State the preparation type.
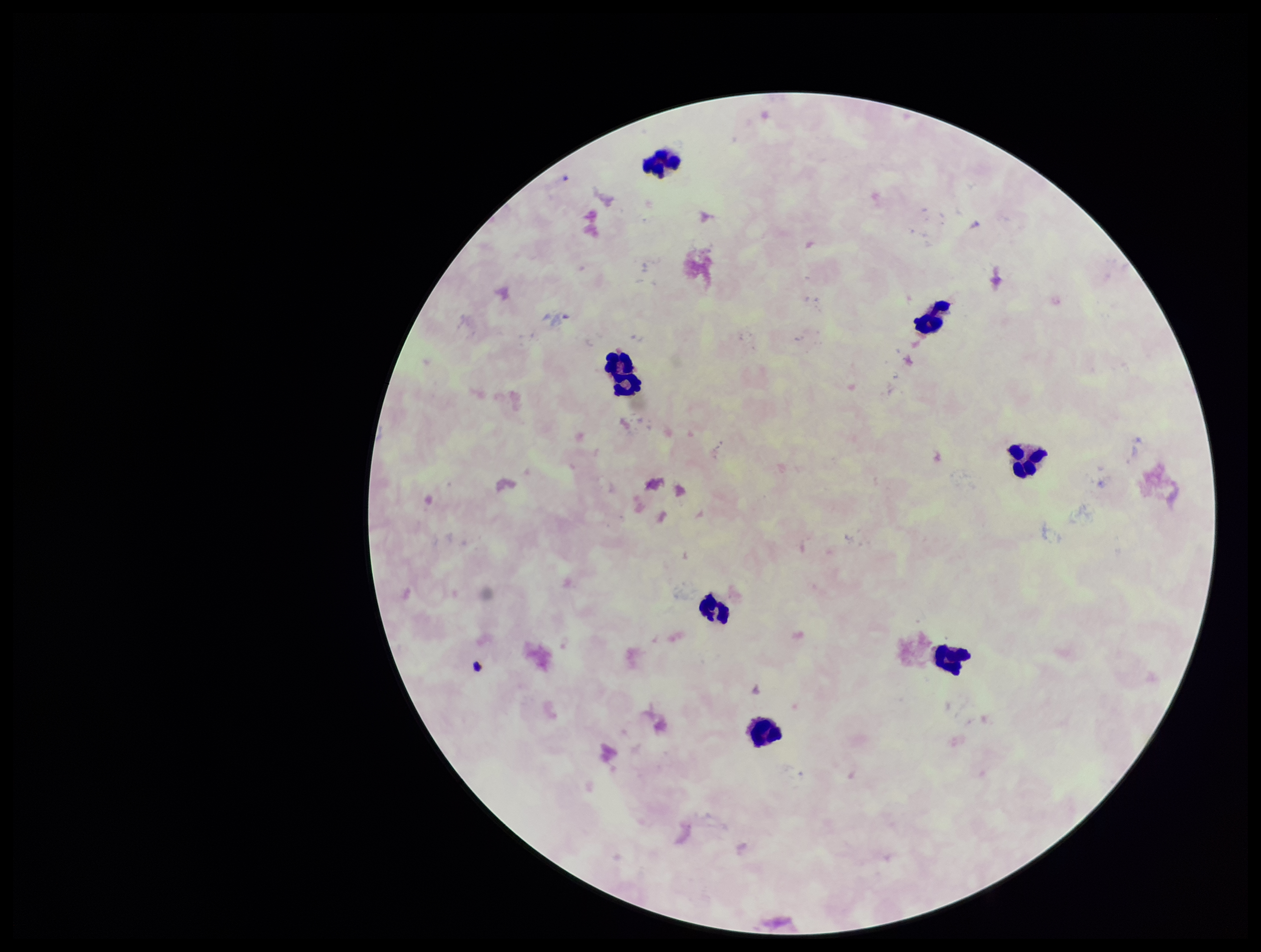

A thick smear.

Stained with Giemsa. Single field of view. Image is 1261×952 pixels. Plasmodium parasites: none identified. Leukocyte count: 7. Parasite count: 0. Patient malaria status: negative. Smartphone photograph taken through the eyepiece of a microscope.